Describe the morphology of the erythrocytes.
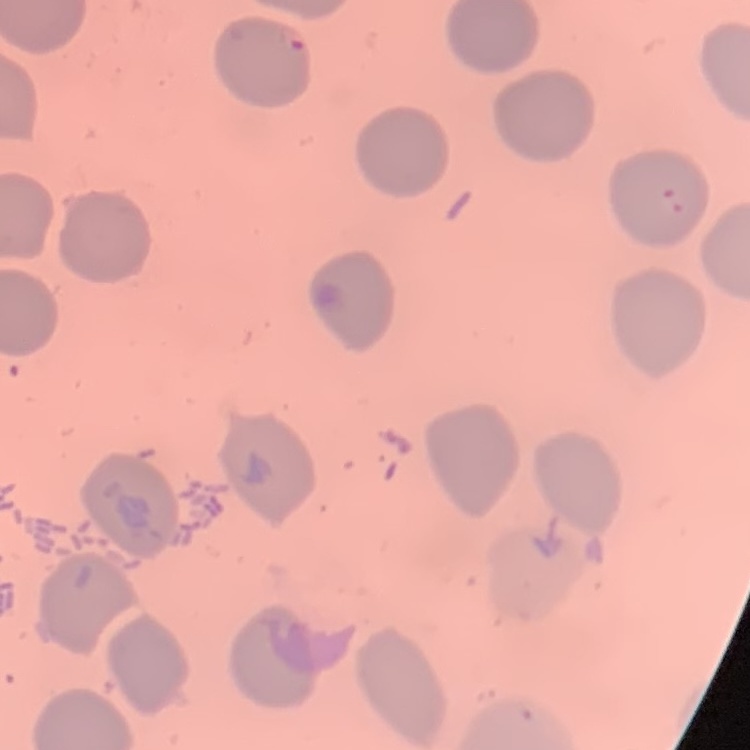

They show no rouleaux formation.

image type = one tile cut from a larger photomicrograph
stain = Field's or Giemsa
preparation = thin blood film